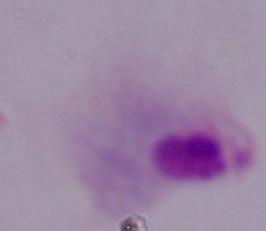

Photomicrograph. Captured at 1000x magnification. A trichomonad is shown.